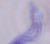

{
  "magnification": "1000x",
  "modality": "micrograph",
  "identification": "trypanosome"
}